Describe the morphology of the erythrocytes.
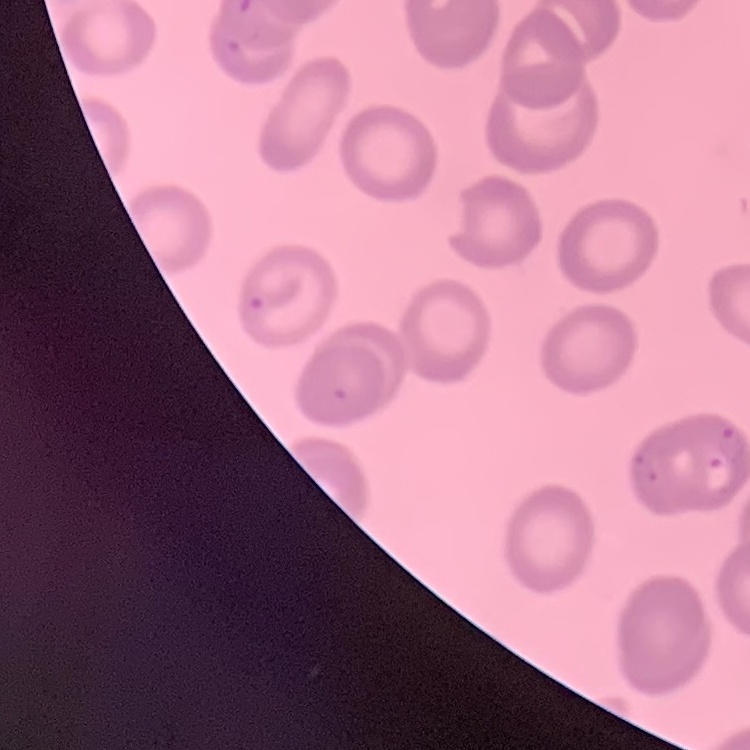

They show no rouleaux formation.

Summary:
  - Image type: one tile cut from a larger photomicrograph
  - Stain: Field's or Giemsa
  - Preparation: thin blood smear